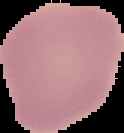

Summary:
  - Image size: 124×133 pixels
  - Preparation: thin blood film
  - Image type: segmented cell region with the area outside set to black
  - Malaria status: uninfected